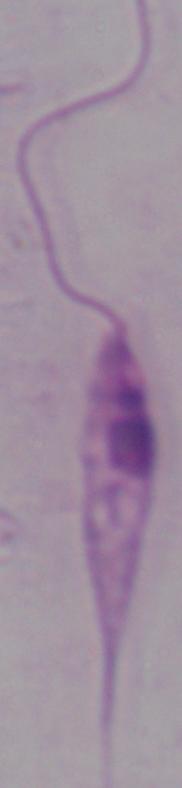
Photomicrograph. A Leishmania parasite is seen. 1000x magnification.